Outline each uninfected red blood cell.
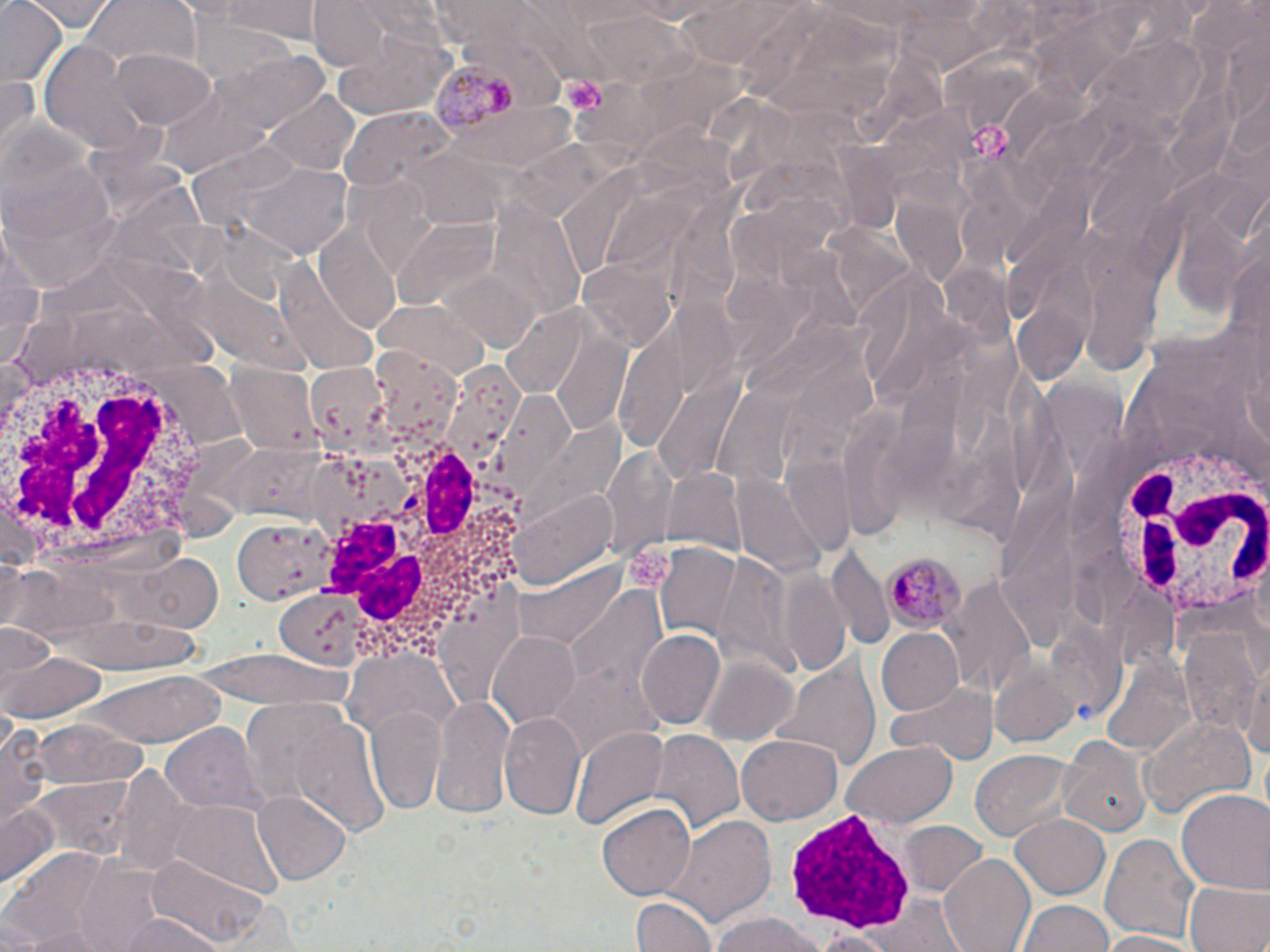

Approximate bounding boxes as (x1, y1, x2, y2) in pixels.
Uninfected red blood cells: (29, 0, 116, 31), (208, 0, 325, 42), (306, 0, 397, 72), (75, 1, 198, 77), (0, 3, 67, 87), (9, 5, 96, 61), (332, 30, 456, 117), (38, 40, 144, 149), (111, 48, 214, 129), (264, 92, 359, 174), (339, 110, 451, 194), (3, 118, 117, 293), (229, 161, 356, 258), (395, 218, 504, 309), (3, 225, 42, 367), (317, 225, 403, 336), (275, 254, 385, 372), (578, 258, 674, 352), (374, 297, 492, 382), (508, 484, 620, 594), (233, 515, 338, 602), (1250, 541, 1270, 655), (117, 549, 224, 634), (947, 572, 1038, 703), (274, 590, 368, 667), (1178, 620, 1263, 738), (874, 627, 964, 716), (636, 630, 725, 729), (486, 631, 583, 727), (0, 645, 108, 722), (770, 647, 879, 773), (1244, 652, 1270, 768), (702, 657, 800, 745), (1097, 657, 1196, 756), (79, 673, 231, 748), (888, 679, 994, 765), (427, 693, 516, 821), (364, 704, 448, 814), (1140, 712, 1254, 818), (500, 713, 586, 819), (2, 717, 50, 831), (28, 717, 144, 791), (164, 724, 260, 812), (571, 728, 668, 830), (648, 730, 744, 836), (1059, 734, 1149, 837), (739, 736, 842, 824), (843, 740, 958, 827), (971, 749, 1075, 843), (1176, 788, 1270, 896), (255, 791, 352, 884), (0, 801, 59, 890), (168, 801, 284, 901), (597, 802, 695, 901), (1012, 814, 1109, 899), (669, 815, 776, 928), (901, 821, 986, 897), (1102, 833, 1200, 943), (2, 848, 133, 946), (77, 855, 168, 945), (149, 855, 272, 949), (939, 856, 1035, 952), (1185, 878, 1269, 952), (631, 895, 718, 952), (1019, 901, 1115, 952), (115, 912, 229, 952), (706, 913, 831, 952), (803, 928, 901, 950), (1098, 930, 1207, 951).

slide-level diagnosis = Plasmodium malariae
modality = optical microscopy
stain = May-Grünwald-Giemsa
platelet locations = approximate bounding boxes as (x1, y1, x2, y2) in pixels: (559, 76, 608, 117), (969, 121, 1014, 162), (627, 539, 678, 590)
Plasmodium malariae-infected red blood cell locations = approximate bounding boxes as (x1, y1, x2, y2) in pixels: (431, 63, 521, 141), (880, 549, 962, 634)
preparation = thin blood film
white blood cell locations = approximate bounding boxes as (x1, y1, x2, y2) in pixels: (0, 337, 235, 579), (1107, 438, 1269, 622), (322, 444, 524, 669), (782, 803, 914, 935)
field of view = one of a larger specimen
magnification = 1000x
image size = 1270×952 pixels